Assess this cell for malaria.
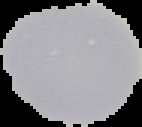

It is uninfected.

Summary:
  - Preparation: thin blood smear
  - Image size: 142×127 pixels
  - Image type: segmented cell region on a black background